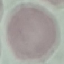

result = negative for malaria parasites
image type = cell patch, automatically extracted from a larger field of view and resized to 64 × 64 pixels
stain = Giemsa
preparation = thin blood film
capture = smartphone through the microscope eyepiece